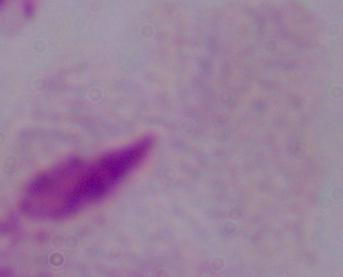 1000x magnification. Photomicrograph. A trichomonad is seen.